Classify this cell by malaria status.
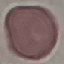

It is uninfected.

Summary:
  - Capture: smartphone through the microscope eyepiece
  - Stain: Giemsa
  - Image type: cell patch, automatically extracted from a larger field of view and resized to 64 × 64 pixels
  - Preparation: thin blood film